Comment on the morphology of the red blood cells.
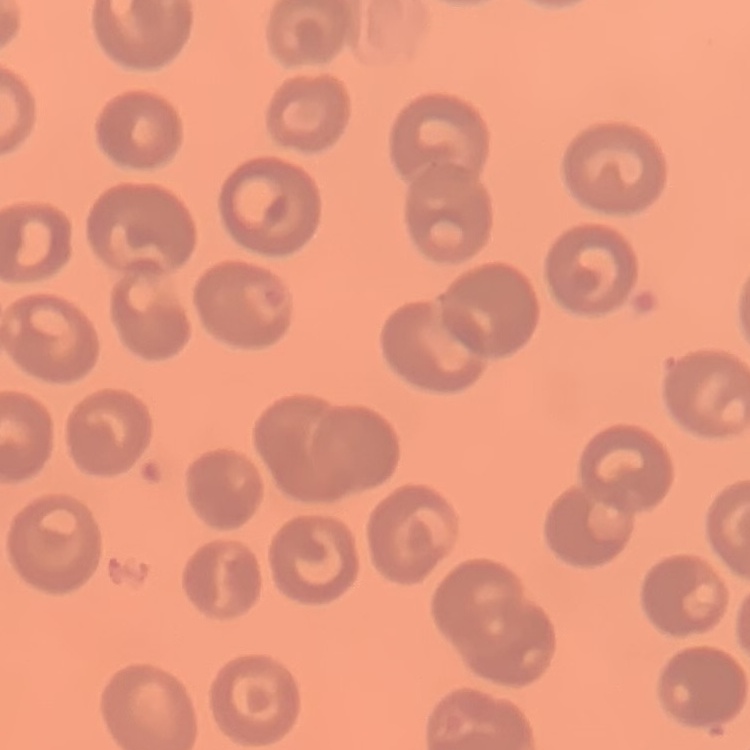
They show no rouleaux formation.

Summary:
  - Preparation: thin peripheral smear
  - Image type: one tile cut from a larger photomicrograph
  - Stain: Field's or Giemsa